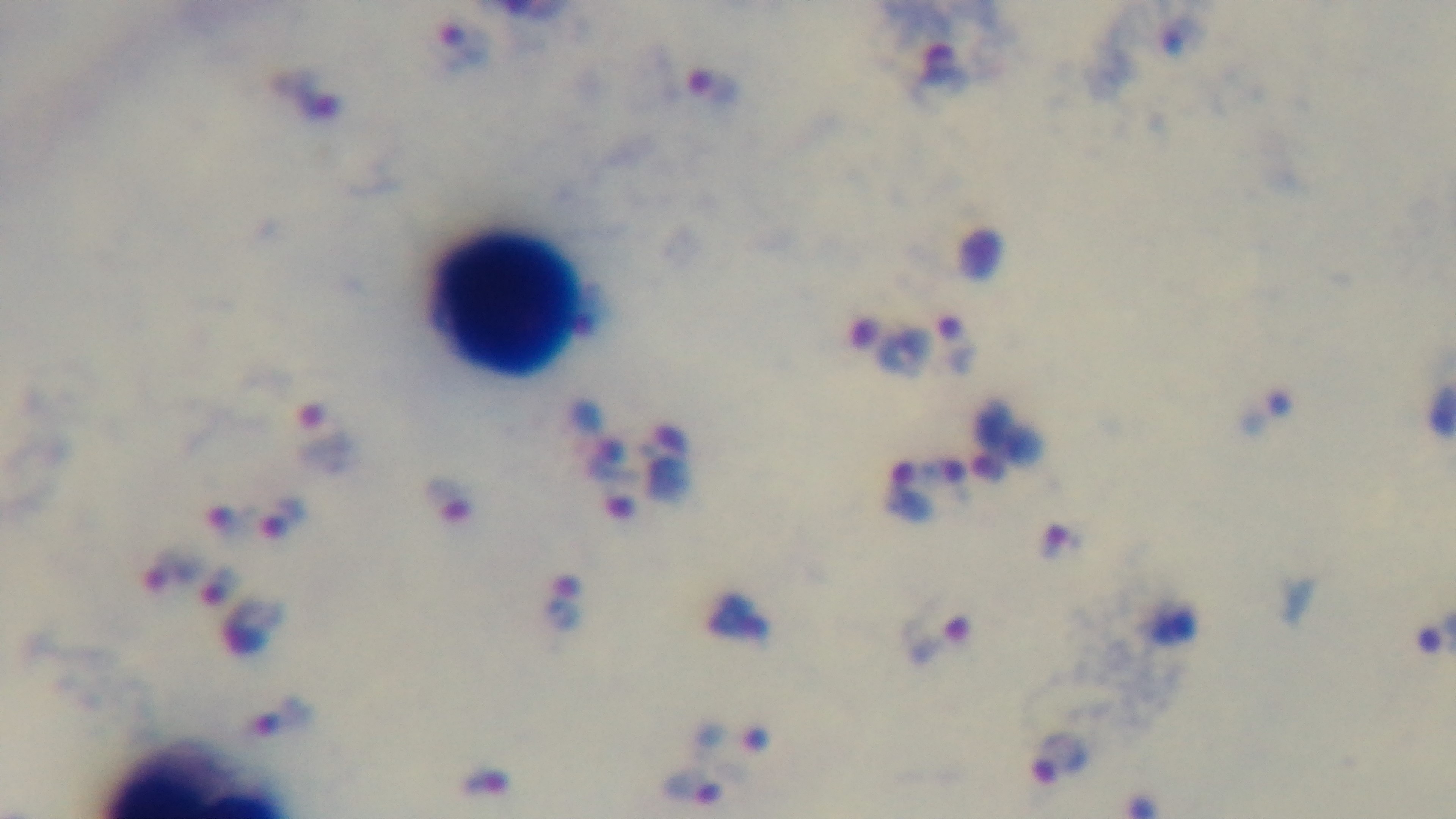

{
  "malaria_status": "infected",
  "objective": "100x oil immersion",
  "field_of_view": "single",
  "stain": "Giemsa",
  "modality": "light microscopy",
  "capture": "mounted 4K digital camera",
  "preparation": "thick smear"
}